Assess the morphology of the erythrocytes.
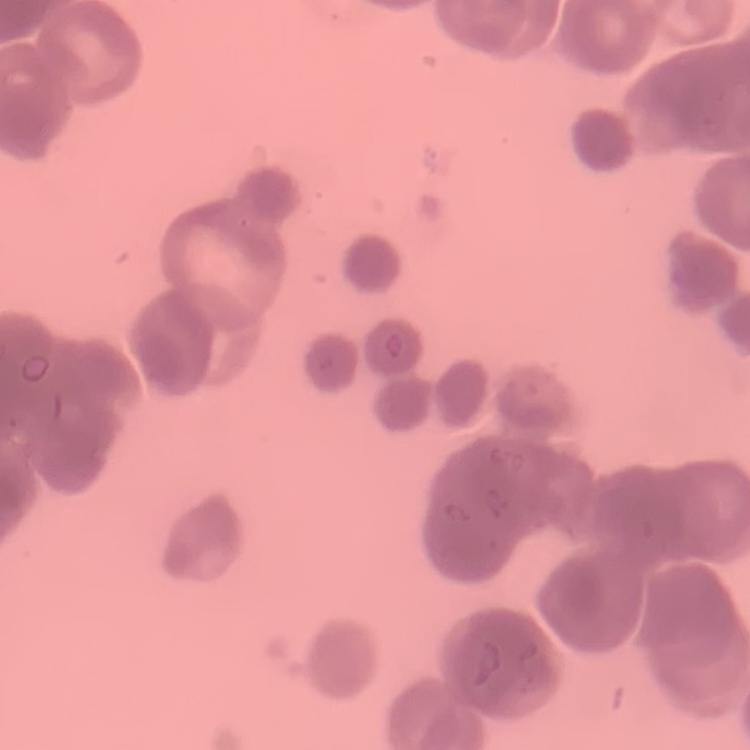

Rouleaux formation.

Summary:
  - Stain: Field's or Giemsa
  - Image type: square crop of a larger photomicrograph
  - Preparation: thin blood film